Outline each uninfected red blood cell.
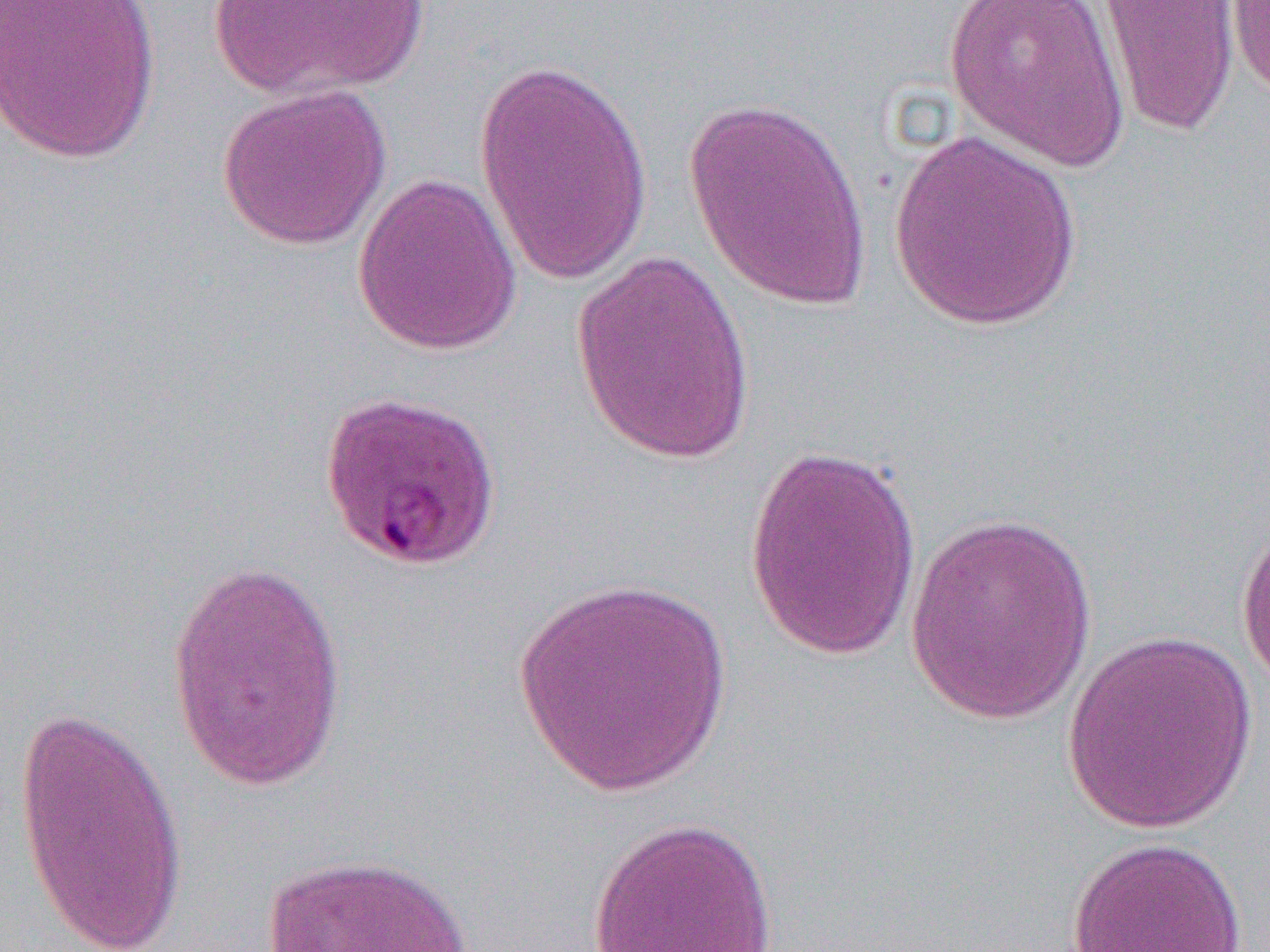
Approximate bounding boxes as named x1/y1/x2/y2 corners in pixels.
Uninfected red blood cells: (x1=0, y1=0, x2=162, y2=165), (x1=942, y1=0, x2=1132, y2=174), (x1=1093, y1=0, x2=1241, y2=139), (x1=1225, y1=0, x2=1270, y2=102), (x1=205, y1=1, x2=429, y2=102), (x1=473, y1=56, x2=654, y2=287), (x1=216, y1=82, x2=391, y2=252), (x1=682, y1=95, x2=873, y2=314), (x1=887, y1=128, x2=1085, y2=331), (x1=353, y1=173, x2=523, y2=356), (x1=570, y1=251, x2=758, y2=466), (x1=742, y1=443, x2=923, y2=662), (x1=904, y1=510, x2=1099, y2=726), (x1=1234, y1=514, x2=1270, y2=695), (x1=164, y1=555, x2=352, y2=798), (x1=512, y1=573, x2=731, y2=797), (x1=1061, y1=628, x2=1259, y2=835), (x1=9, y1=705, x2=188, y2=952), (x1=587, y1=815, x2=781, y2=952), (x1=1066, y1=836, x2=1248, y2=952), (x1=261, y1=852, x2=476, y2=952).

Summary:
  - Slide-level diagnosis: Plasmodium falciparum
  - Magnification: 1000x
  - Modality: light microscopy
  - Field of view: single
  - Image size: 1270×952 pixels
  - Preparation: thin blood film